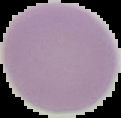

Summary:
  - Preparation: thin blood film
  - Image type: segmented cell region with the area outside set to black
  - Malaria status: uninfected
  - Image size: 121×118 pixels